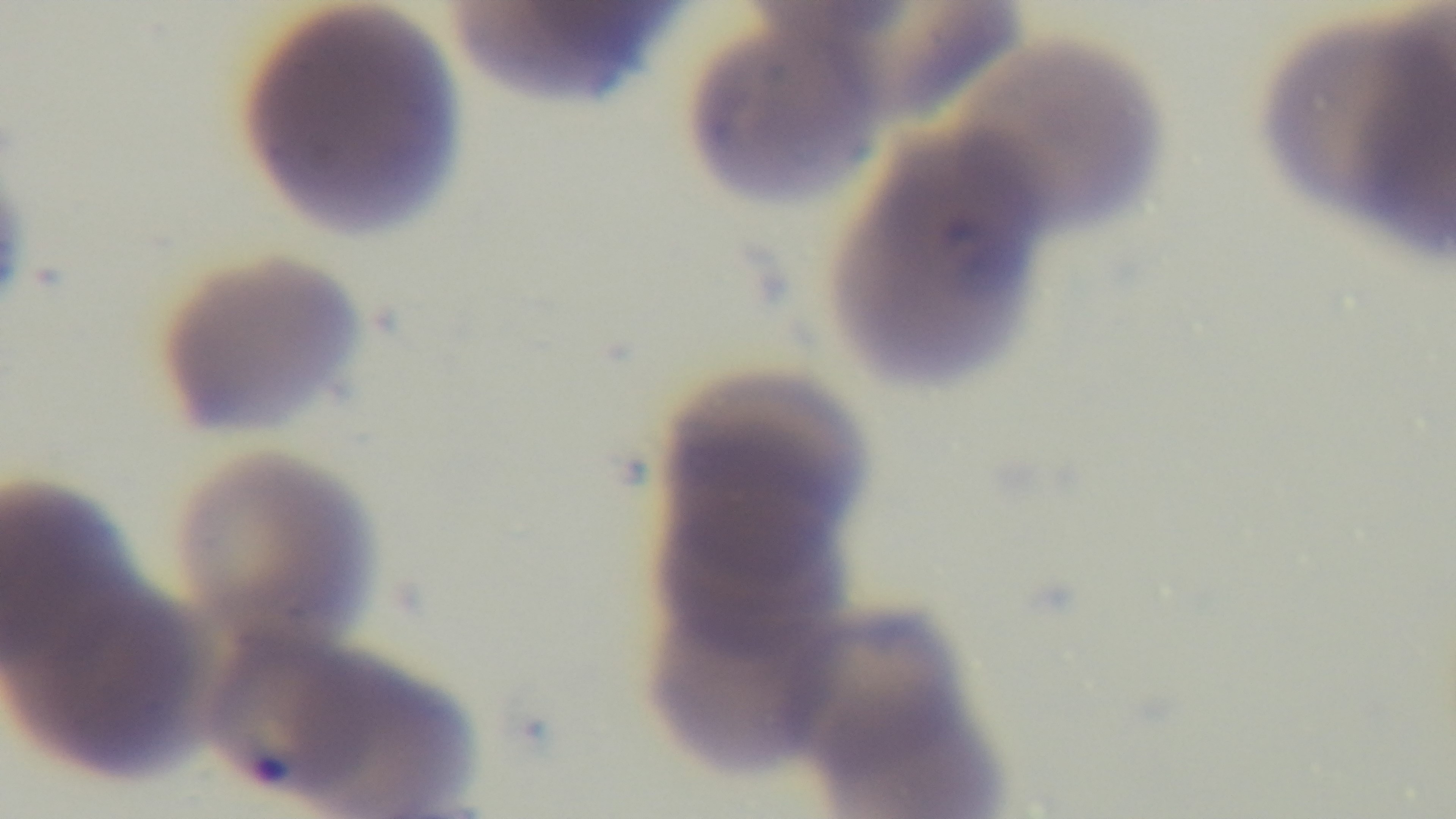 100x oil-immersion objective. Captured with a mounted 4K digital camera. Photomicrograph. Giemsa-stained. Preparation: thin. Malaria status: positive. One field from the slide.